Report the malaria status of this cell.
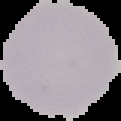
It is uninfected.

image_type: cell region segmented out of the field of view; surrounding area masked to black
preparation: thin blood smear
image_size: 121×121 pixels